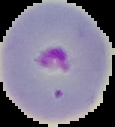

malaria_status: parasitized
preparation: thin blood smear
image_size: 115×127 pixels
image_type: segmented cell region with the area outside set to black